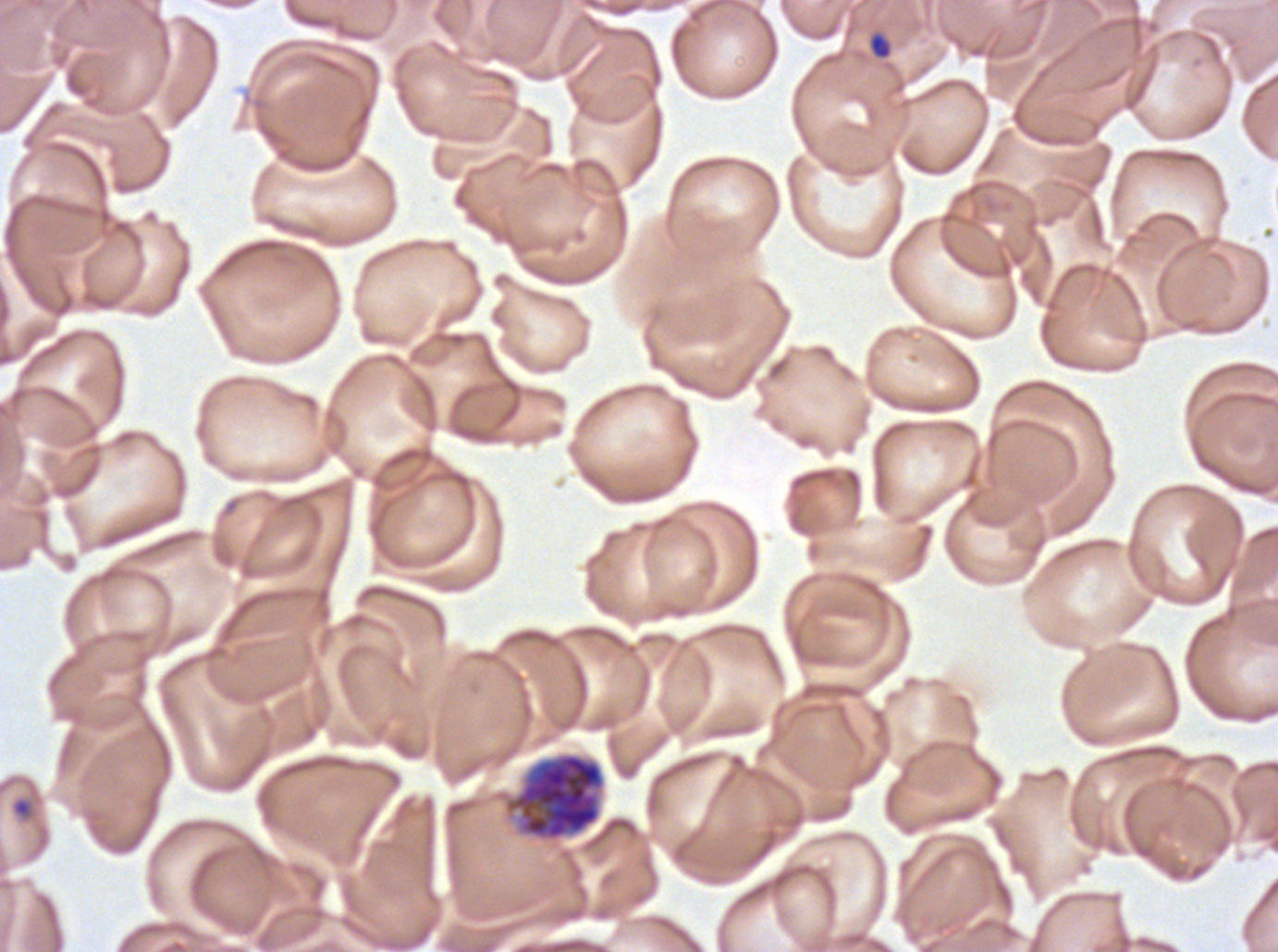
Approximate bounding boxes as {x1, y1, x2, y2} in pixels.
Summary:
  - Early schizont locations: {503, 751, 606, 842}
  - Ring locations: {868, 33, 891, 59}, {11, 798, 32, 818}
  - Specimen: ex-vivo P. falciparum culture from a patient in The Gambia, grown for 24 to 48 hours
  - Stain: Giemsa
  - Field of view: sub-image separated from a larger composite
  - Image size: 1278×952 pixels
  - Life-cycle stages observed: ring, early schizont
  - Preparation: thin blood film